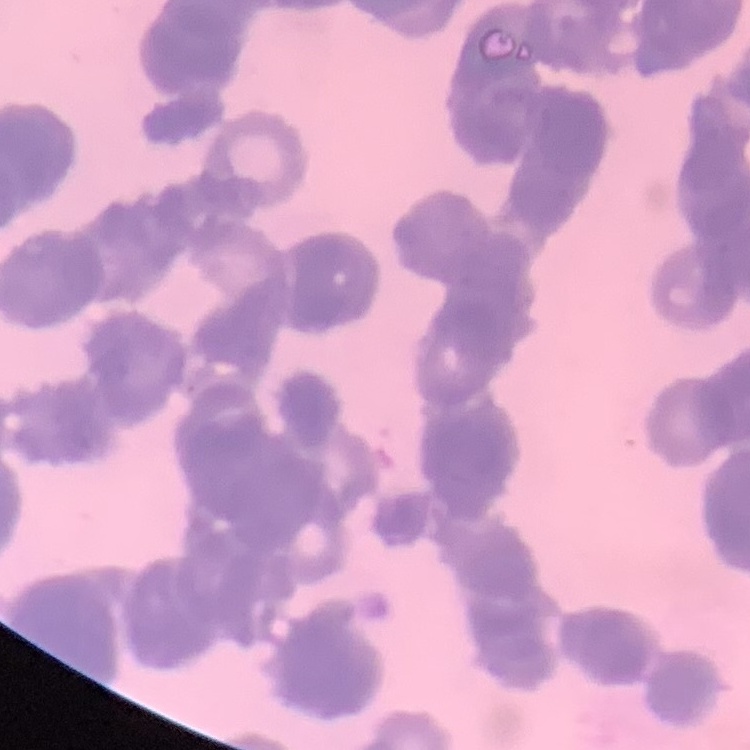
Summary:
  - Erythrocyte morphology: rouleaux formation
  - Preparation: thin peripheral smear
  - Stain: Field's or Giemsa
  - Image type: one tile cut from a larger photomicrograph